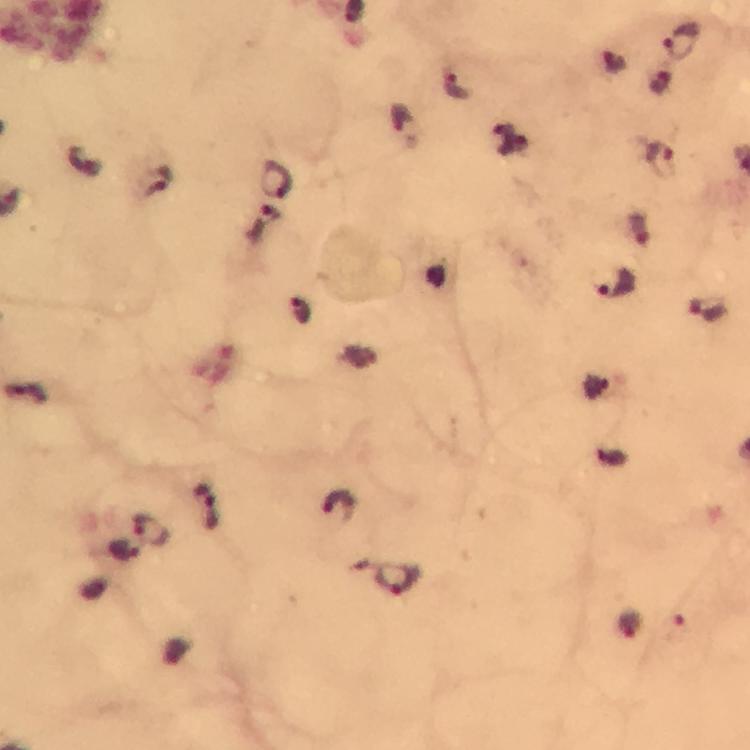

Approximate centers as {x, y} in pixels. Malaria parasite locations: {683, 42}, {454, 85}, {401, 121}, {659, 156}, {278, 181}, {163, 183}, {617, 284}, {299, 306}, {707, 312}, {207, 504}, {339, 505}, {152, 531}, {126, 548}, {398, 582}. From a diagnostic examination for malaria. Thick blood smear. Immersion oil applied. 100x magnification. Cropped region of a single field of view. Photographed with a smartphone mounted on the microscope. Giemsa-stained preparation. Image is 750×750 pixels.